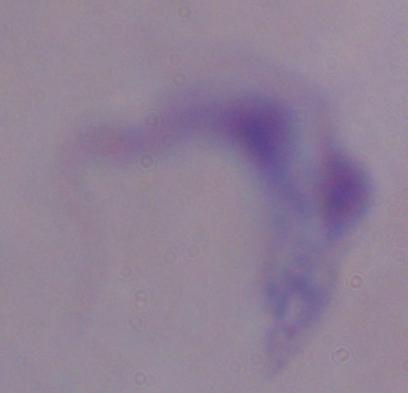

magnification = 1000x
identification = trypanosome
modality = micrograph